Assess the morphology of the erythrocytes.
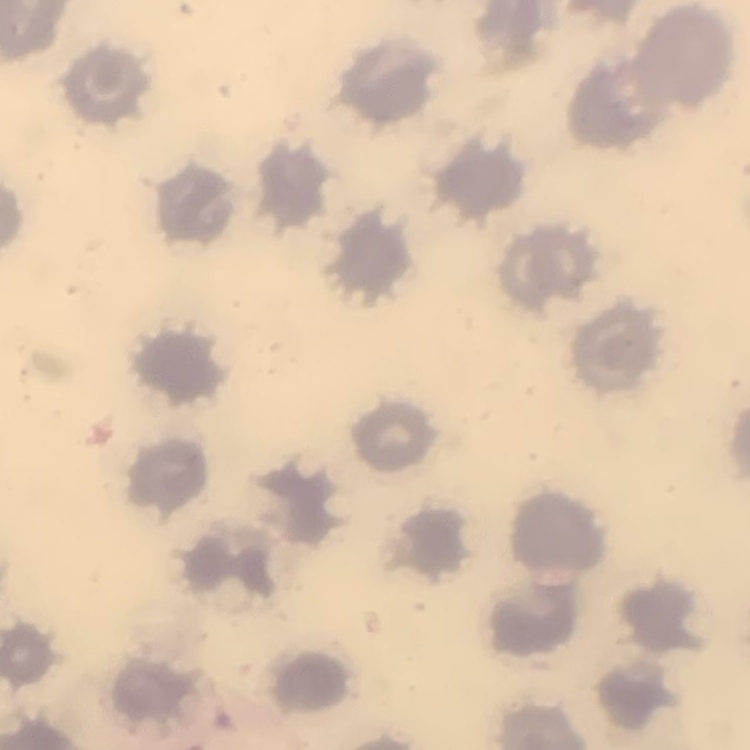
They show no rouleaux formation.

image type = square crop of a larger photomicrograph
stain = Field's or Giemsa
preparation = thin blood smear